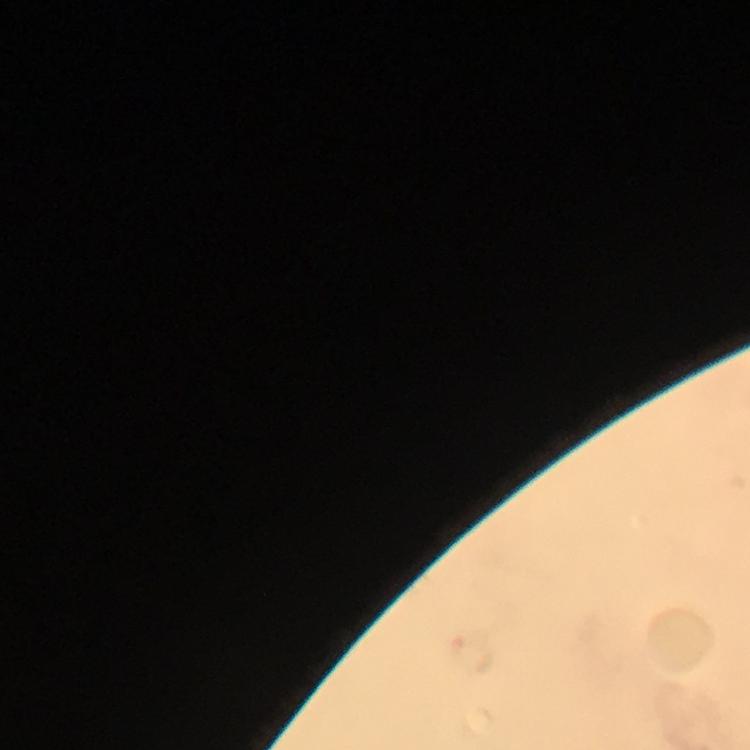

Approximate centers as (x, y) in pixels.
Summary:
  - Plasmodium parasite locations: (475, 652)
  - Magnification: 100x
  - Cropped from: a single field of view
  - Context: from a diagnostic examination for malaria
  - Immersion oil: used
  - Preparation: thick blood smear
  - Capture: smartphone camera through the microscope
  - Image size: 750×750 pixels
  - Stain: Giemsa